Name the parasite shown.
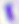

Toxoplasma gondii.

magnification: 400x
modality: micrograph